Locate every blood parasite and identify its species.
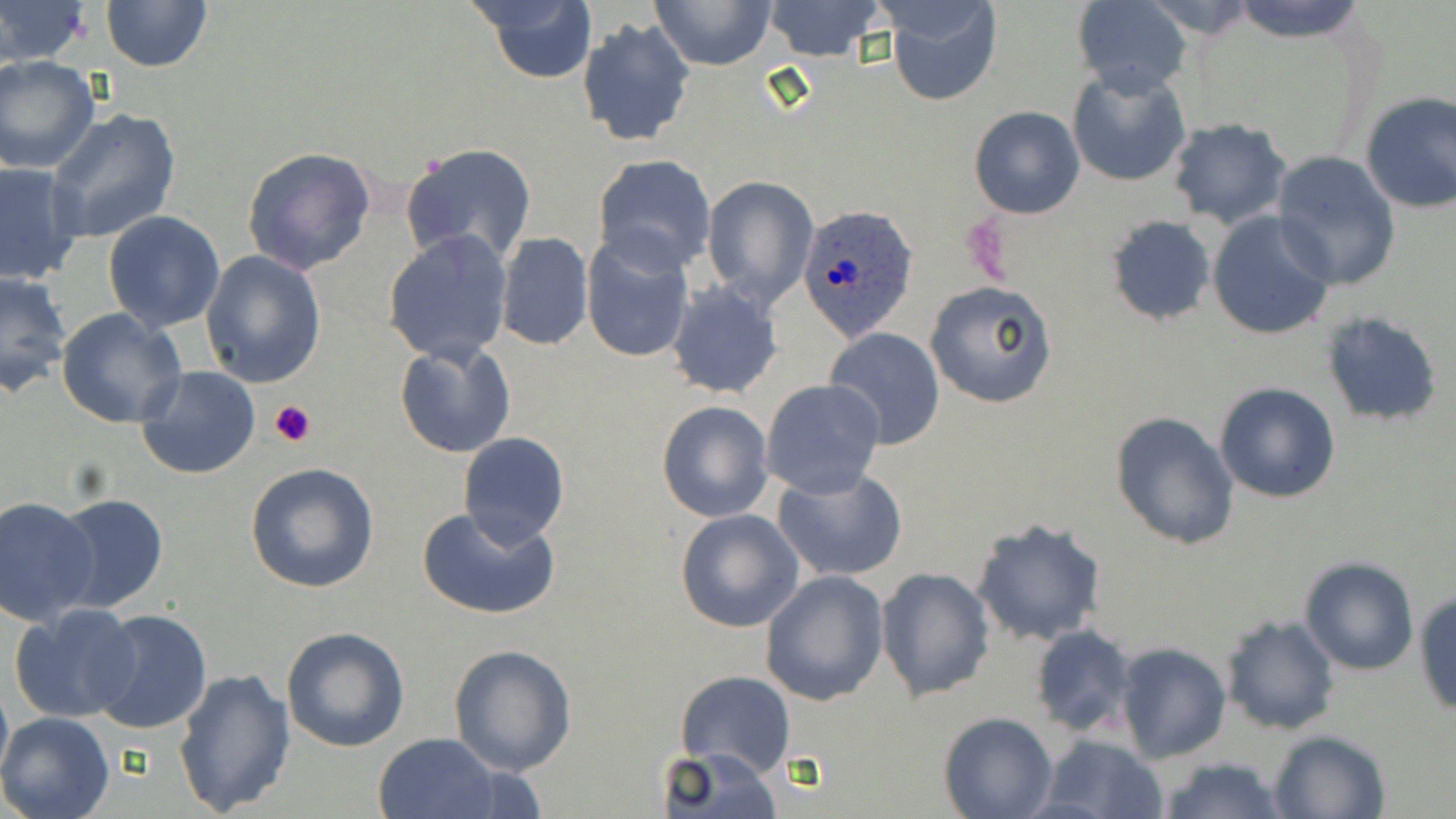

Approximate bounding boxes as [x1, y1, x2, y2] in pixels.
Plasmodium ovale-infected red blood cells (subset): [799, 202, 917, 340].
No Plasmodium falciparum, Plasmodium malariae, Plasmodium vivax, Babesia divergens, or Trypanosoma brucei observed.

Platelet locations: [269, 398, 317, 446]. Uninfected red blood cell locations (subset): [1, 0, 91, 66], [650, 0, 777, 71], [761, 0, 886, 62], [884, 0, 1001, 108], [1073, 0, 1192, 98], [1228, 0, 1367, 43], [100, 1, 213, 73], [1143, 1, 1262, 38], [468, 2, 599, 85], [577, 17, 696, 148], [1, 55, 101, 174], [1066, 68, 1192, 189], [1358, 90, 1456, 214], [968, 105, 1086, 219], [45, 106, 182, 245], [1165, 118, 1290, 229], [399, 141, 537, 269], [241, 146, 377, 275], [1269, 153, 1400, 292], [592, 154, 716, 275], [0, 160, 85, 285], [701, 175, 818, 308], [102, 211, 227, 332], [1207, 213, 1336, 340], [1105, 215, 1217, 325], [383, 230, 512, 366], [494, 232, 594, 351], [581, 234, 695, 363], [200, 250, 327, 388], [0, 270, 73, 396], [925, 280, 1058, 409], [665, 283, 784, 398], [56, 308, 185, 429], [823, 327, 946, 448], [394, 340, 515, 459], [137, 364, 262, 481], [761, 380, 885, 498], [1213, 381, 1341, 504], [656, 400, 773, 522], [1110, 411, 1241, 549], [459, 432, 569, 549], [246, 462, 381, 594], [772, 467, 910, 583], [52, 493, 169, 612], [1, 495, 99, 624], [418, 506, 561, 619], [674, 509, 804, 631], [970, 518, 1108, 646], [1301, 558, 1418, 676], [876, 566, 994, 702], [761, 570, 890, 706], [1413, 588, 1456, 715], [8, 602, 136, 723], [87, 608, 213, 736], [1221, 616, 1339, 736], [1029, 624, 1140, 739], [282, 626, 411, 752], [448, 643, 578, 776], [1115, 643, 1232, 764], [173, 668, 296, 815], [675, 670, 796, 777], [0, 673, 12, 790], [0, 712, 117, 819], [938, 712, 1056, 819], [1267, 729, 1390, 818], [370, 733, 502, 819], [1036, 734, 1170, 819], [660, 747, 782, 819], [1156, 756, 1288, 819]. Slide-level diagnosis: Plasmodium ovale. One field of a larger specimen. Light microscopy. Thin blood film. Image is 1456×819 pixels. 1000x magnification. May-Grünwald-Giemsa stain.